State which parasite is depicted.
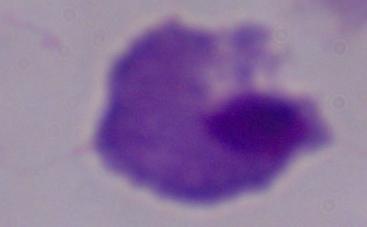
A trichomonad.

magnification = 1000x
modality = photomicrograph